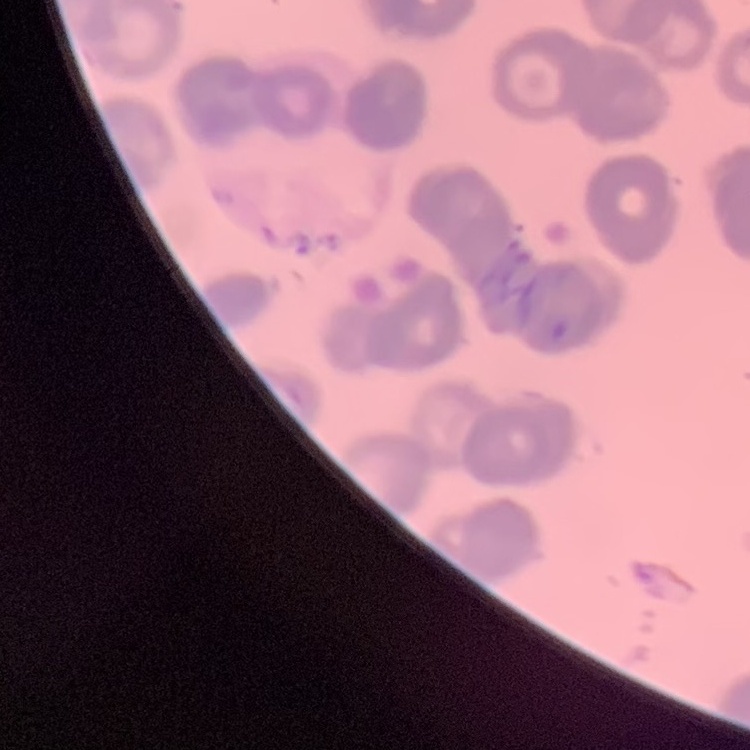

erythrocyte morphology = rouleaux formation
stain = Field's or Giemsa
image type = one tile cut from a larger photomicrograph
preparation = thin blood smear